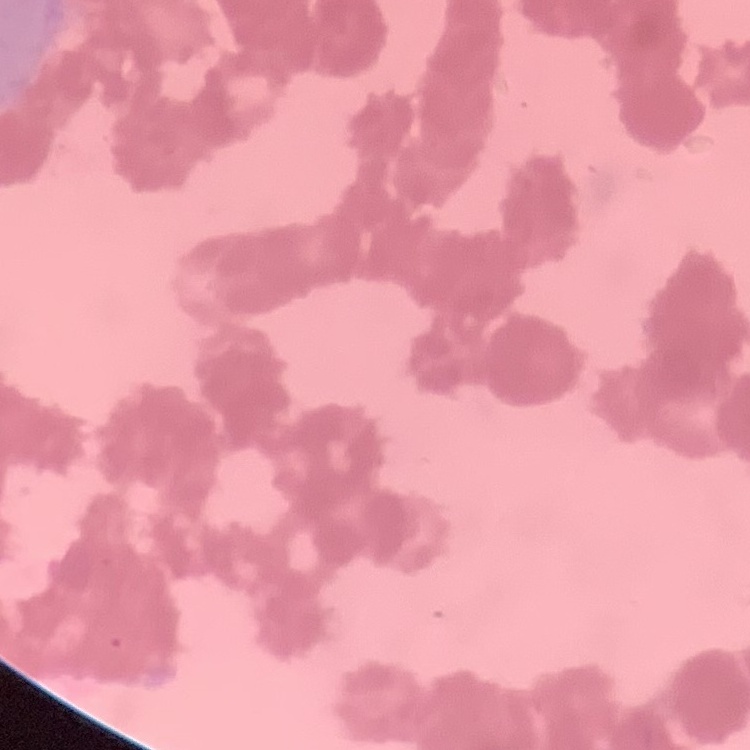

The erythrocytes show rouleaux formation. One tile cut from a larger photomicrograph. Thin peripheral smear. Stained with either Field's or Giemsa.